Classify this cell by malaria status.
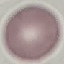

It is uninfected.

{
  "capture": "smartphone camera at the microscope eyepiece",
  "preparation": "thin blood smear",
  "image_type": "automatically extracted cell patch, resized to 64 × 64 pixels",
  "stain": "Giemsa"
}